Report the malaria status of this cell.
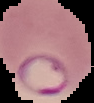

It is parasitized.

preparation = thin blood film
image type = segmented cell region with the area outside set to black
image size = 94×103 pixels